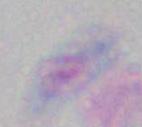

Summary:
  - Modality: micrograph
  - Magnification: 1000x
  - Identification: Toxoplasma gondii